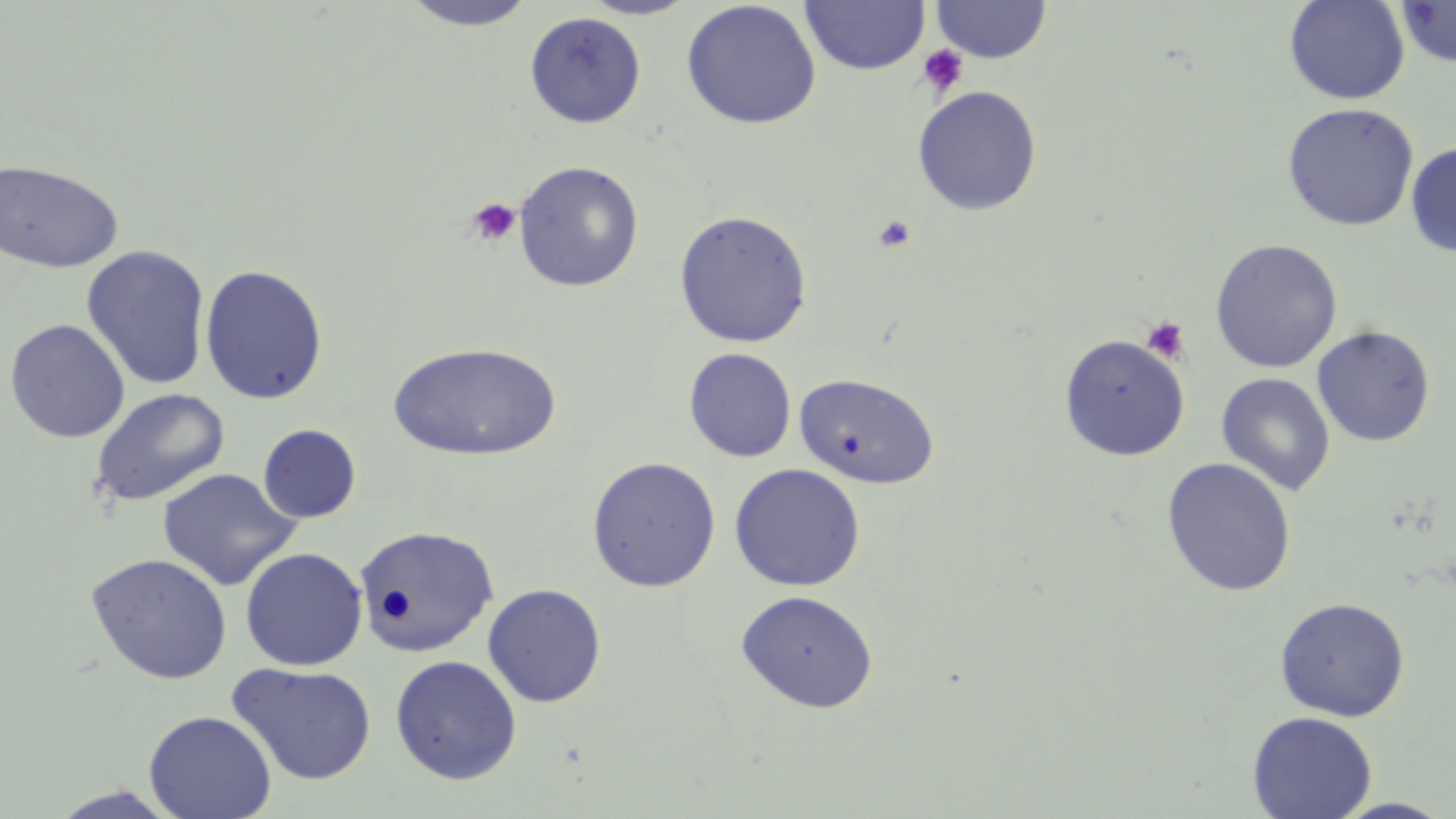 Approximate bounding boxes as named x1/y1/x2/y2 corners in pixels. Uninfected red blood cell locations: (x1=800, y1=0, x2=931, y2=75), (x1=930, y1=0, x2=1053, y2=63), (x1=1284, y1=0, x2=1410, y2=105), (x1=400, y1=1, x2=540, y2=31), (x1=580, y1=1, x2=698, y2=20), (x1=681, y1=1, x2=821, y2=129), (x1=1396, y1=1, x2=1456, y2=68), (x1=524, y1=11, x2=647, y2=128), (x1=913, y1=85, x2=1042, y2=216), (x1=1282, y1=102, x2=1419, y2=231), (x1=1405, y1=142, x2=1456, y2=257), (x1=0, y1=158, x2=124, y2=273), (x1=513, y1=160, x2=645, y2=292), (x1=674, y1=209, x2=812, y2=347), (x1=1209, y1=238, x2=1343, y2=373), (x1=81, y1=245, x2=211, y2=390), (x1=200, y1=264, x2=328, y2=405), (x1=4, y1=318, x2=130, y2=443), (x1=1312, y1=325, x2=1436, y2=446), (x1=1058, y1=333, x2=1190, y2=461), (x1=388, y1=342, x2=563, y2=462), (x1=684, y1=348, x2=797, y2=462), (x1=794, y1=372, x2=940, y2=489), (x1=1216, y1=372, x2=1335, y2=496), (x1=90, y1=388, x2=230, y2=507), (x1=258, y1=423, x2=361, y2=523), (x1=586, y1=456, x2=722, y2=592), (x1=1161, y1=457, x2=1297, y2=596), (x1=729, y1=463, x2=866, y2=592), (x1=158, y1=468, x2=301, y2=590), (x1=356, y1=524, x2=499, y2=658), (x1=240, y1=547, x2=368, y2=671), (x1=86, y1=553, x2=233, y2=684), (x1=482, y1=583, x2=607, y2=707), (x1=735, y1=589, x2=879, y2=714), (x1=1274, y1=597, x2=1410, y2=721), (x1=390, y1=655, x2=522, y2=784), (x1=226, y1=661, x2=378, y2=785), (x1=144, y1=710, x2=276, y2=819), (x1=1247, y1=710, x2=1377, y2=819), (x1=43, y1=784, x2=184, y2=818), (x1=1329, y1=797, x2=1456, y2=818). Platelet locations: (x1=917, y1=45, x2=969, y2=98), (x1=465, y1=197, x2=521, y2=247), (x1=872, y1=213, x2=917, y2=253), (x1=1140, y1=315, x2=1190, y2=364). Slide-level diagnosis: no evidence of blood parasites. Optical microscopy. Captured at 1000x magnification. Image is 1456×819 pixels. May-Grünwald-Giemsa-stained preparation. Thin blood film. One field of a larger specimen.